Give the extent of all Babesia divergens-infected red blood cells.
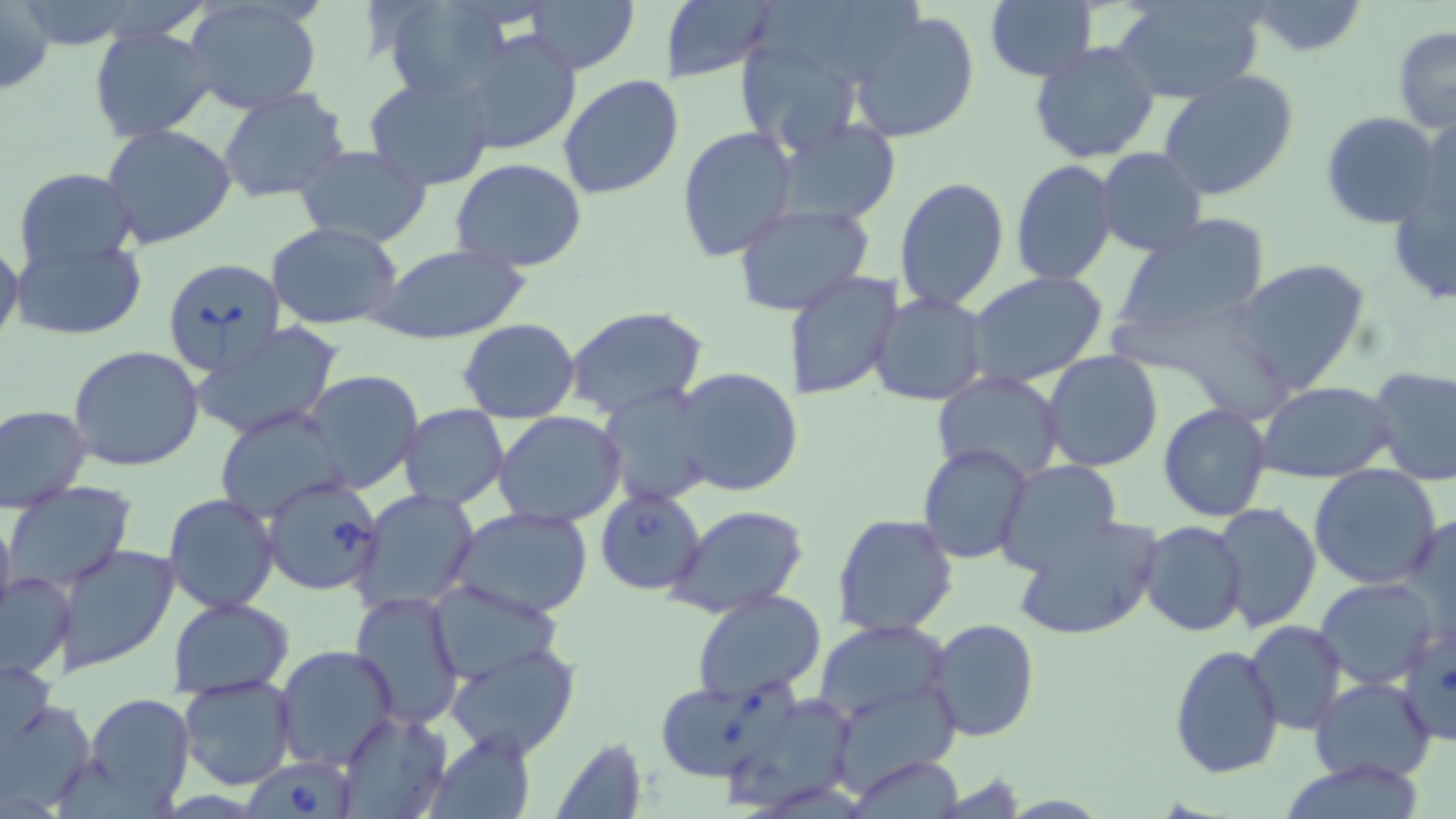
Approximate bounding boxes as (x1, y1, x2, y2) in pixels.
Babesia divergens-infected red blood cells: (160, 255, 286, 375), (261, 475, 384, 597), (595, 487, 707, 596), (655, 682, 789, 782), (245, 756, 356, 819).

slide_level_diagnosis: Babesia divergens
image_size: 1456×819 pixels
magnification: 1000x
field_of_view: one of a larger specimen
uninfected_red_blood_cell_locations: 'approximate bounding boxes as (x1, y1, x2, y2) in pixels: (384, 0, 517, 104), (523, 0, 641, 74), (1112, 0, 1267, 104), (183, 1, 323, 114), (1247, 1, 1367, 56), (0, 2, 56, 100), (660, 2, 775, 82), (986, 2, 1097, 80), (848, 9, 980, 145), (88, 26, 220, 142), (1392, 27, 1456, 133), (456, 29, 582, 158), (731, 34, 864, 161), (1029, 40, 1160, 163), (1157, 71, 1300, 202), (557, 73, 685, 201), (364, 76, 495, 189), (217, 88, 351, 204), (1320, 111, 1443, 230), (1417, 111, 1454, 228), (775, 119, 902, 225), (101, 123, 237, 250), (678, 126, 798, 263), (294, 145, 433, 247), (1096, 148, 1207, 257), (450, 158, 589, 273), (1010, 159, 1119, 285), (14, 167, 140, 273), (1387, 172, 1455, 310), (894, 176, 1010, 311), (733, 201, 877, 317), (1110, 215, 1270, 347), (265, 222, 406, 330), (10, 237, 149, 340), (0, 242, 24, 352), (377, 244, 528, 345), (1232, 258, 1371, 395), (786, 270, 904, 401), (967, 271, 1109, 389), (871, 292, 990, 407), (1107, 303, 1293, 418), (566, 308, 708, 421), (459, 318, 580, 422), (192, 324, 345, 441), (68, 345, 205, 471), (1043, 351, 1164, 473), (1368, 365, 1456, 485), (672, 367, 803, 499), (298, 371, 423, 494), (933, 371, 1066, 483), (1257, 382, 1396, 484), (598, 387, 720, 509), (1158, 403, 1272, 521), (0, 404, 92, 512), (398, 404, 509, 510), (212, 405, 352, 525), (494, 413, 626, 527), (917, 443, 1033, 565), (996, 460, 1123, 574), (1309, 465, 1441, 590), (6, 482, 134, 596), (352, 488, 481, 614), (162, 492, 281, 615), (1212, 503, 1322, 632), (668, 505, 810, 620), (454, 508, 594, 620), (0, 509, 16, 630), (1403, 509, 1456, 638), (831, 514, 958, 638), (1013, 514, 1164, 643), (1138, 520, 1249, 638), (55, 543, 181, 673), (0, 570, 75, 680), (1316, 577, 1440, 690), (427, 580, 561, 683), (693, 590, 827, 703), (351, 591, 464, 729), (168, 598, 294, 697), (812, 618, 956, 730), (926, 618, 1041, 742), (1246, 620, 1347, 735), (1398, 625, 1455, 747), (446, 643, 581, 760), (274, 644, 399, 771), (1169, 644, 1284, 778), (0, 653, 57, 763), (178, 674, 299, 791), (1310, 676, 1437, 784), (82, 691, 196, 814), (0, 692, 96, 812), (337, 710, 452, 818), (430, 729, 538, 818), (552, 737, 646, 818), (845, 757, 967, 817), (1278, 757, 1431, 818)'
stain: May-Grünwald-Giemsa
modality: light microscopy
preparation: thin blood smear